Outline each blood parasite and name the species.
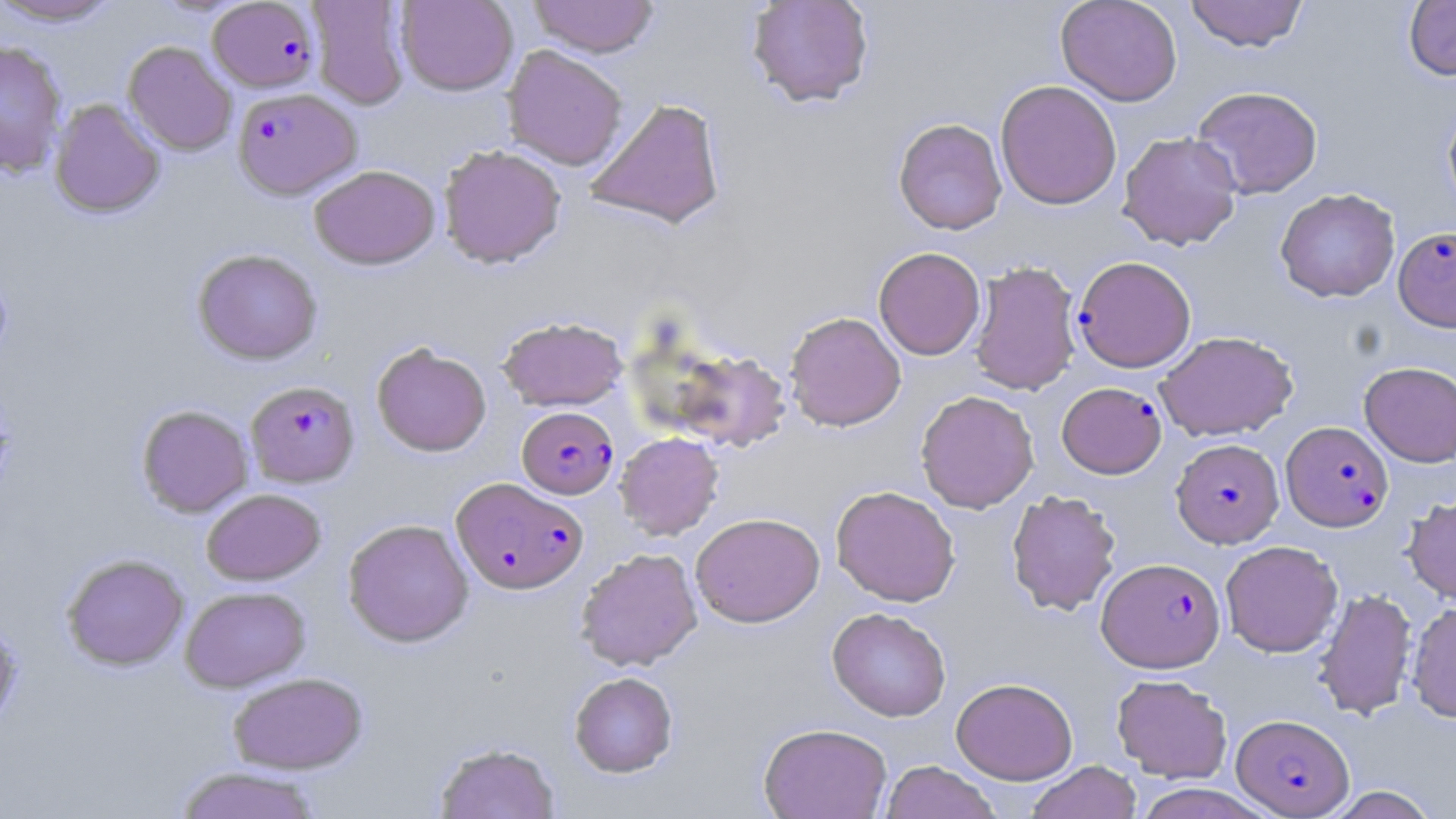
Approximate bounding boxes as named x1/y1/x2/y2 corners in pixels.
Plasmodium falciparum-infected red blood cells (subset): (x1=208, y1=1, x2=320, y2=92), (x1=233, y1=87, x2=361, y2=199), (x1=1393, y1=226, x2=1456, y2=331), (x1=246, y1=380, x2=360, y2=487), (x1=1056, y1=382, x2=1167, y2=479), (x1=517, y1=406, x2=619, y2=498), (x1=1282, y1=421, x2=1393, y2=531), (x1=1172, y1=439, x2=1284, y2=547), (x1=452, y1=477, x2=588, y2=594), (x1=1097, y1=557, x2=1226, y2=672), (x1=1232, y1=714, x2=1354, y2=817).
No Plasmodium ovale, Plasmodium malariae, Plasmodium vivax, Babesia divergens, or Trypanosoma brucei observed.

slide-level diagnosis = Plasmodium falciparum
magnification = 1000x
uninfected red blood cell locations (subset) = approximate bounding boxes as named x1/y1/x2/y2 corners in pixels: (x1=0, y1=0, x2=121, y2=26), (x1=397, y1=0, x2=518, y2=96), (x1=529, y1=0, x2=659, y2=58), (x1=746, y1=0, x2=874, y2=108), (x1=1055, y1=0, x2=1183, y2=106), (x1=1184, y1=0, x2=1309, y2=52), (x1=1404, y1=0, x2=1456, y2=80), (x1=307, y1=1, x2=411, y2=109), (x1=0, y1=41, x2=68, y2=177), (x1=123, y1=41, x2=236, y2=156), (x1=502, y1=45, x2=628, y2=170), (x1=995, y1=80, x2=1122, y2=209), (x1=1191, y1=85, x2=1323, y2=199), (x1=584, y1=97, x2=726, y2=230), (x1=49, y1=99, x2=165, y2=218), (x1=1442, y1=99, x2=1456, y2=217), (x1=893, y1=117, x2=1007, y2=235), (x1=1118, y1=131, x2=1243, y2=251), (x1=438, y1=144, x2=566, y2=268), (x1=308, y1=164, x2=441, y2=270), (x1=1275, y1=188, x2=1400, y2=302), (x1=873, y1=247, x2=986, y2=360), (x1=192, y1=248, x2=322, y2=365), (x1=968, y1=259, x2=1082, y2=395), (x1=784, y1=311, x2=906, y2=431), (x1=498, y1=316, x2=627, y2=411), (x1=1155, y1=331, x2=1298, y2=441), (x1=371, y1=342, x2=491, y2=457), (x1=670, y1=349, x2=791, y2=452), (x1=1359, y1=361, x2=1456, y2=466), (x1=915, y1=390, x2=1039, y2=513), (x1=136, y1=404, x2=253, y2=518), (x1=614, y1=432, x2=724, y2=540), (x1=831, y1=485, x2=960, y2=606), (x1=202, y1=488, x2=325, y2=585), (x1=1006, y1=489, x2=1121, y2=615), (x1=1402, y1=494, x2=1456, y2=605), (x1=690, y1=512, x2=825, y2=627), (x1=342, y1=518, x2=474, y2=647), (x1=1220, y1=540, x2=1343, y2=657), (x1=576, y1=548, x2=702, y2=671), (x1=61, y1=553, x2=190, y2=671), (x1=180, y1=586, x2=310, y2=691), (x1=1313, y1=588, x2=1417, y2=720), (x1=1406, y1=600, x2=1456, y2=723), (x1=827, y1=607, x2=951, y2=722), (x1=0, y1=615, x2=23, y2=733), (x1=569, y1=671, x2=678, y2=777), (x1=227, y1=672, x2=368, y2=774), (x1=1111, y1=674, x2=1232, y2=783), (x1=951, y1=678, x2=1078, y2=784), (x1=758, y1=722, x2=892, y2=819), (x1=434, y1=742, x2=560, y2=819), (x1=881, y1=760, x2=1000, y2=819), (x1=1026, y1=760, x2=1141, y2=819), (x1=173, y1=766, x2=325, y2=819), (x1=1132, y1=783, x2=1275, y2=819), (x1=1325, y1=785, x2=1440, y2=818)
modality = light microscopy
field of view = single
stain = May-Grünwald-Giemsa
preparation = thin blood film
image size = 1456×819 pixels